Describe the morphology of the erythrocytes.
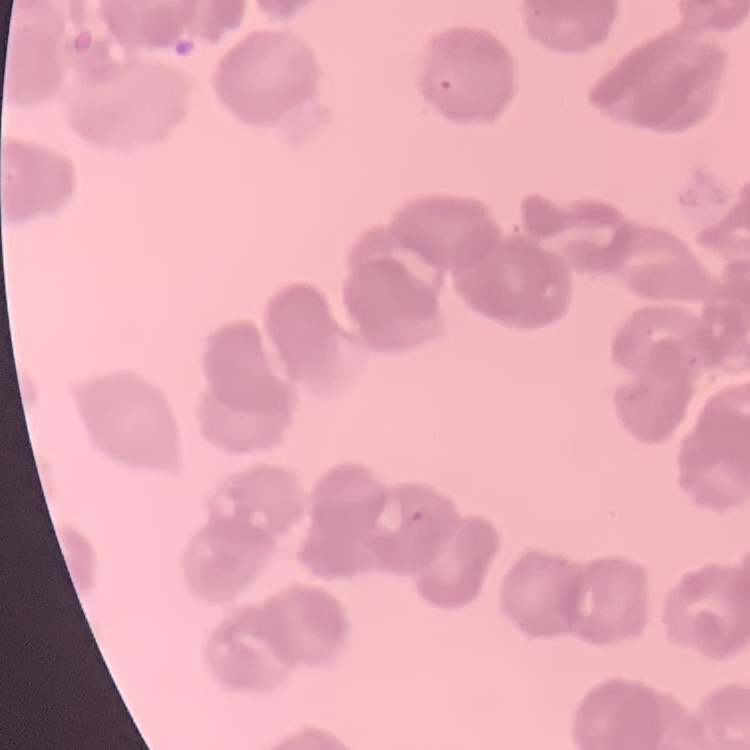

They show rouleaux formation.

image type = square crop of a larger photomicrograph
preparation = thin blood smear
stain = Field's or Giemsa